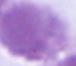
identification = red blood cell
magnification = 1000x
modality = photomicrograph